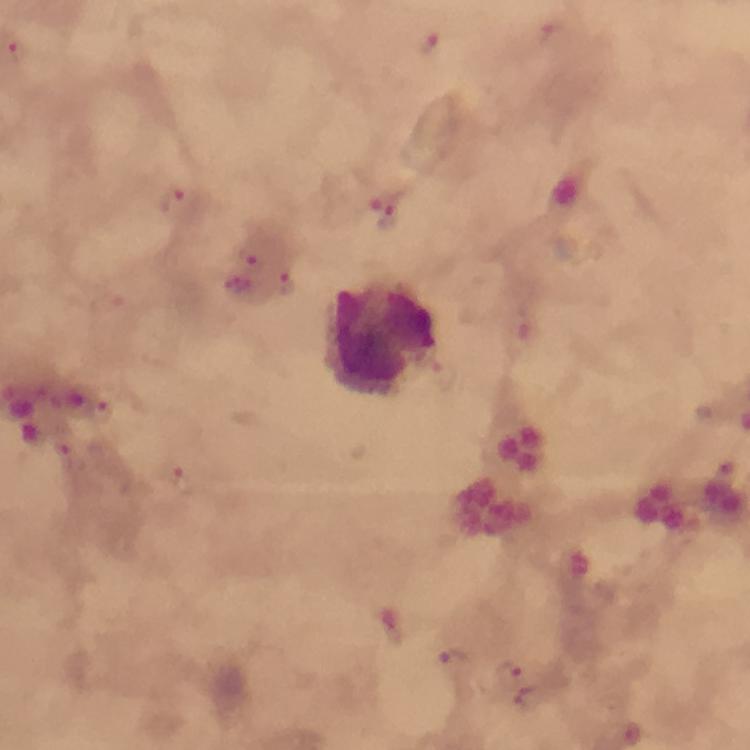
Approximate centers as (x, y) in pixels.
Summary:
  - Plasmodium parasite locations: (551, 34), (428, 42), (15, 51), (173, 198), (388, 213), (249, 255), (288, 283), (103, 404), (66, 446), (454, 658), (509, 672)
  - Leukocyte locations: (382, 341)
  - Stain: Giemsa
  - Cropped from: one field of view
  - Preparation: thick blood film
  - Capture: smartphone camera through the microscope
  - Image size: 750×750 pixels
  - Immersion oil: applied
  - Context: from a diagnostic examination for malaria
  - Magnification: 100x